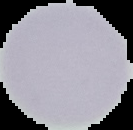
Summary:
  - Image type: segmented cell region with the area outside set to black
  - Image size: 133×130 pixels
  - Preparation: thin blood smear
  - Malaria status: uninfected